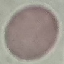

result = no malaria parasites seen
preparation = thin blood film
image type = cell patch, automatically extracted from a larger field of view and resized to 64 × 64 pixels
capture = smartphone camera at the microscope eyepiece
stain = Giemsa